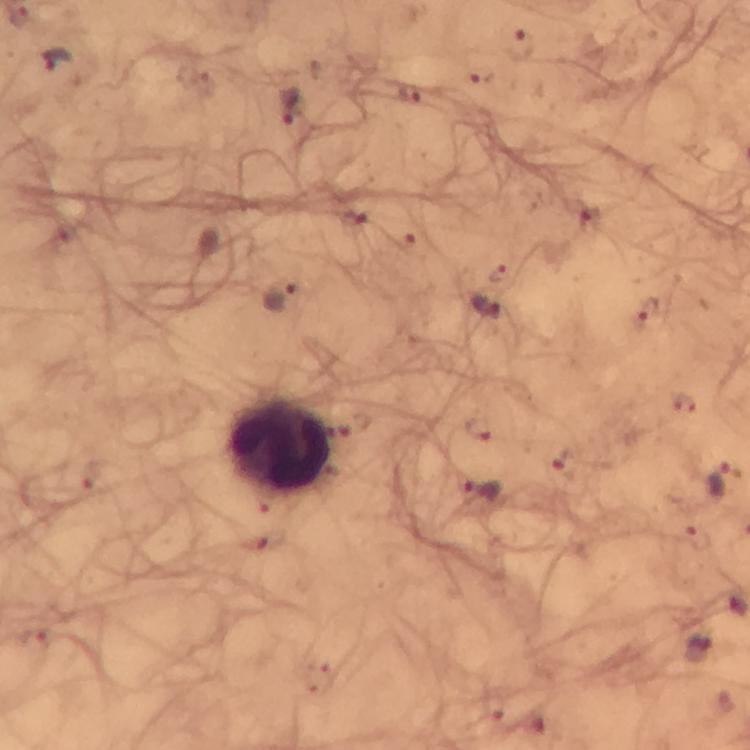

capture = smartphone camera through the microscope
preparation = thick blood film
stain = Giemsa
leukocyte locations = approximate centers as [x, y] in pixels: [279, 446]
cropped from = one field of view
magnification = 100x
context = from a malaria diagnostic workup
immersion oil = used
image size = 750×750 pixels
Plasmodium parasite locations = approximate centers as [x, y] in pixels: [520, 45], [57, 61], [411, 96], [288, 108], [280, 297], [485, 308], [722, 481], [482, 490], [699, 651]